Report the malaria status of this cell.
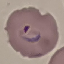

Parasitized.

image type = automatically extracted cell patch, resized to 64 × 64 pixels
capture = smartphone through the microscope eyepiece
preparation = thin blood smear
stain = Giemsa